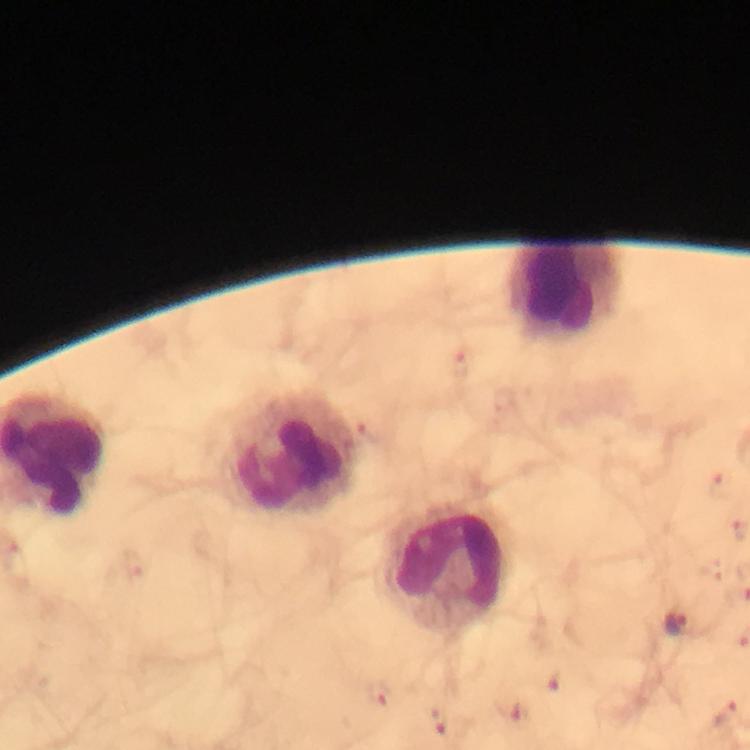
Approximate centers as [x, y] in pixels. Plasmodium parasite locations: [717, 482], [678, 627], [379, 693], [726, 715], [439, 720]. Leukocyte locations: [565, 289], [292, 457], [447, 572]. From a diagnostic examination for malaria. Immersion oil was used. Thick smear. Giemsa-stained preparation. Image is 750×750 pixels. A crop from one field of view. At 100x magnification. Photographed through the microscope with a smartphone camera.